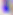
Toxoplasma gondii is seen. Captured at 400x magnification. Photomicrograph.